Report the malaria status of this cell.
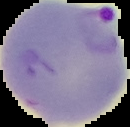

It is parasitized.

Summary:
  - Image type: segmented cell region with the area outside set to black
  - Image size: 130×127 pixels
  - Preparation: thin blood smear